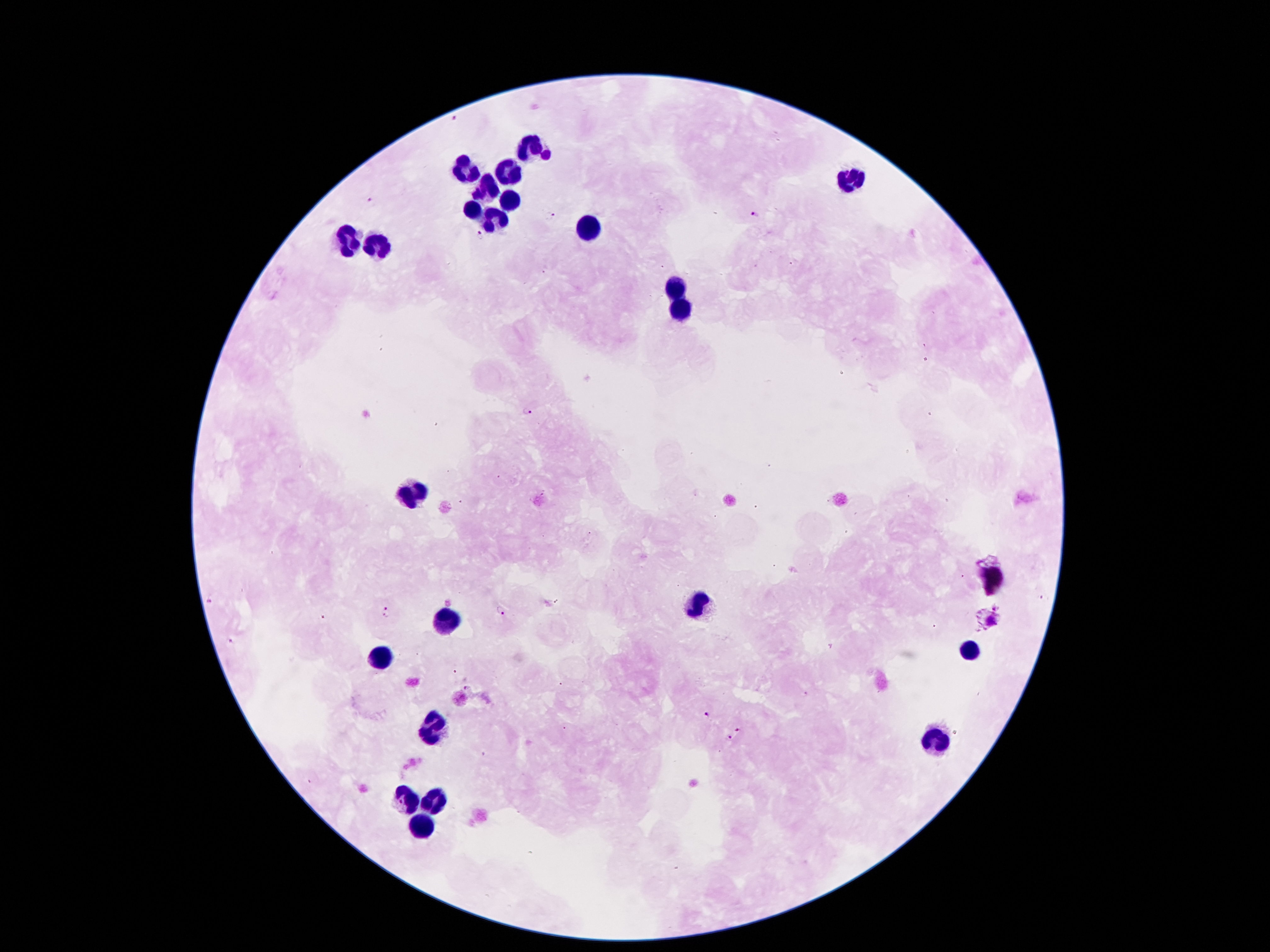
coordinate format = approximate centers as [x, y] in pixels
leukocyte locations = [534, 144], [465, 168], [509, 173], [851, 180], [485, 190], [512, 201], [472, 211], [498, 217], [584, 226], [349, 241], [378, 244], [677, 290], [683, 308], [414, 494], [695, 604], [446, 621], [970, 648], [379, 661], [436, 727], [934, 744], [433, 800], [408, 801], [422, 827]
malaria parasite locations = [457, 117], [371, 202], [549, 216], [755, 216], [481, 235], [527, 409], [208, 602], [386, 610], [499, 610], [232, 641], [470, 689], [707, 713], [739, 731], [730, 736]
magnification = 100x
preparation = thick blood film
capture = smartphone through the microscope eyepiece
stain = Giemsa
patient malaria status = infected with Plasmodium falciparum
image size = 1270×952 pixels
field of view = one from this slide